State the blood parasite species.
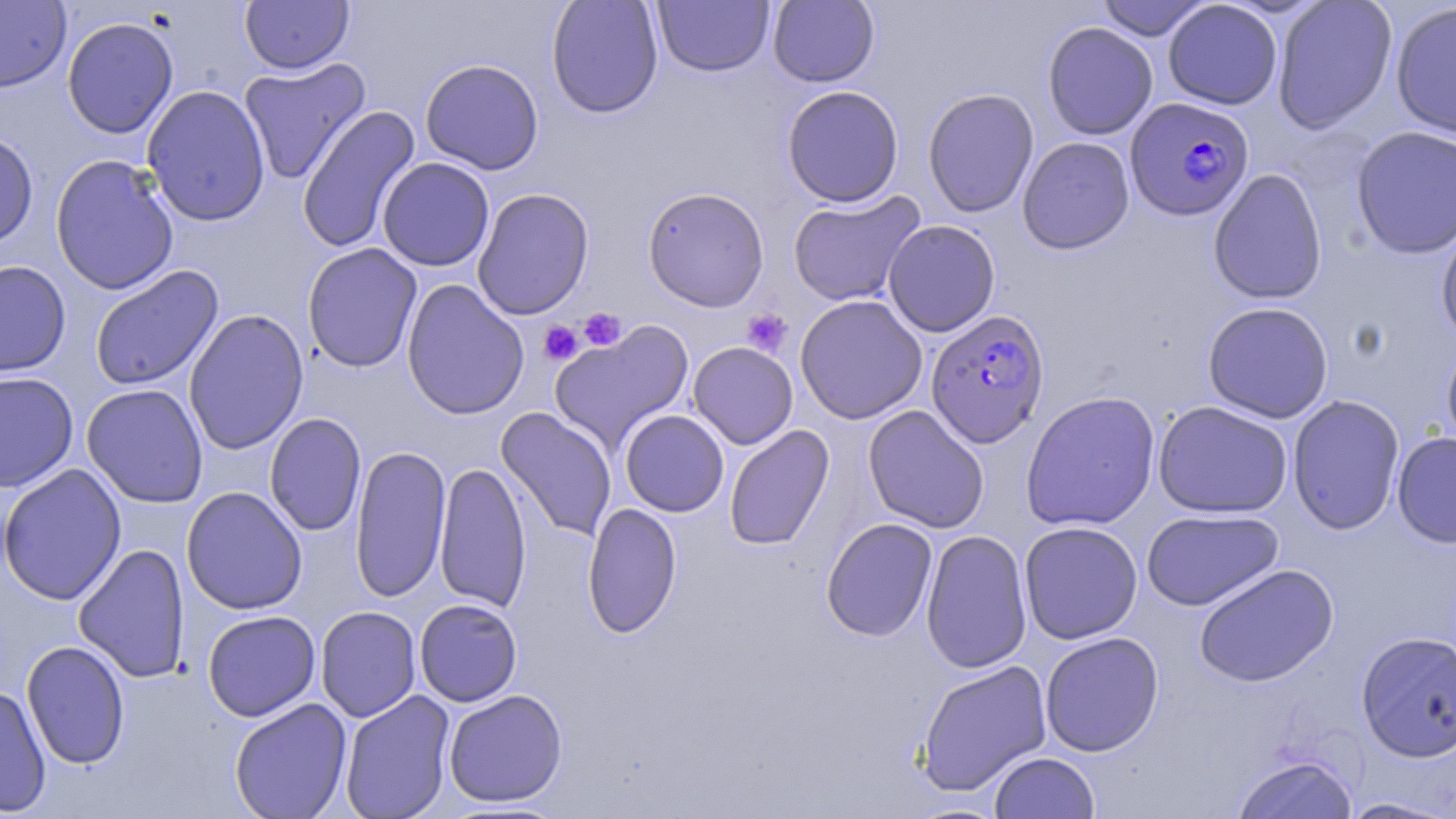
Plasmodium falciparum.

Summary:
  - Coordinate format: approximate bounding boxes as [x1, y1, x2, y2] in pixels
  - Uninfected red blood cell locations: [0, 0, 71, 93], [240, 0, 354, 75], [546, 0, 664, 118], [767, 0, 879, 87], [1095, 0, 1213, 41], [1272, 0, 1398, 134], [652, 1, 774, 76], [1163, 1, 1283, 110], [1390, 1, 1456, 140], [771, 2, 885, 183], [62, 16, 179, 139], [1042, 21, 1158, 140], [237, 57, 371, 184], [420, 59, 544, 175], [142, 84, 271, 227], [781, 85, 904, 207], [922, 88, 1039, 218], [297, 105, 422, 254], [1351, 125, 1456, 259], [0, 130, 39, 251], [1017, 136, 1135, 254], [50, 154, 179, 296], [377, 157, 494, 271], [1208, 168, 1328, 304], [642, 186, 769, 312], [472, 187, 595, 321], [787, 190, 926, 307], [1436, 218, 1456, 348], [883, 220, 1000, 337], [302, 243, 422, 372], [0, 260, 71, 377], [89, 265, 224, 391], [401, 279, 529, 420], [795, 295, 927, 425], [1202, 302, 1334, 423], [184, 308, 309, 455], [549, 321, 695, 453], [1441, 337, 1456, 459], [688, 342, 798, 449], [0, 371, 79, 493], [81, 384, 209, 507], [1020, 391, 1161, 531], [1287, 394, 1405, 535], [1152, 400, 1293, 519], [862, 404, 990, 534], [496, 407, 617, 542], [619, 410, 729, 517], [264, 413, 366, 537], [724, 425, 834, 551], [1392, 431, 1456, 547], [349, 445, 452, 603], [435, 461, 531, 613], [0, 463, 127, 605], [181, 486, 307, 614], [582, 502, 682, 638], [1141, 508, 1284, 611], [821, 518, 938, 642], [1019, 521, 1143, 644], [920, 529, 1032, 674], [73, 542, 191, 684], [1194, 563, 1339, 687], [414, 598, 523, 707], [315, 606, 421, 722], [202, 610, 320, 722], [1356, 630, 1456, 762], [1040, 631, 1164, 756], [21, 640, 130, 769], [916, 659, 1052, 796], [0, 684, 52, 816], [442, 689, 568, 807], [340, 690, 456, 819], [229, 698, 353, 819], [989, 751, 1099, 818], [1231, 754, 1358, 819], [1336, 797, 1455, 818]
  - Platelet locations: [578, 308, 627, 351], [741, 309, 792, 357], [539, 321, 583, 365]
  - Plasmodium falciparum-infected red blood cell locations: [1125, 97, 1255, 221], [925, 309, 1050, 448]
  - Preparation: thin blood smear
  - Field of view: single
  - Image size: 1456×819 pixels
  - Stain: May-Grünwald-Giemsa
  - Magnification: 1000x
  - Modality: light microscopy